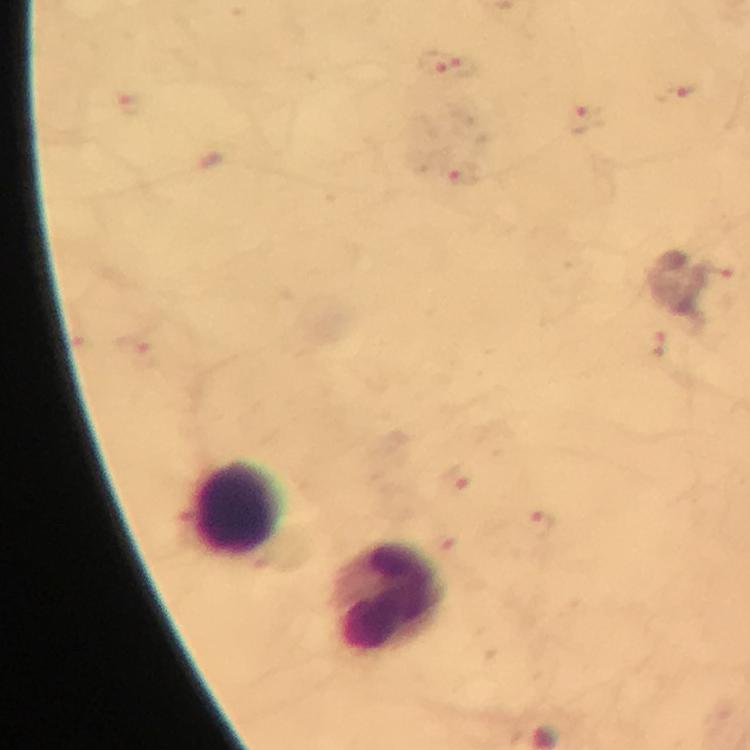 Approximate centers as {x, y} in pixels. Leukocyte locations: {236, 507}, {388, 597}. Malaria parasite locations: {433, 61}, {463, 65}, {582, 120}, {465, 176}. Thick blood smear. Immersion oil was used. At 100x magnification. Cropped region of a single field of view. Giemsa-stained preparation. Image is 750×750 pixels. From a diagnostic examination for malaria. Photographed with a smartphone mounted on the microscope.